Report the malaria status of this cell.
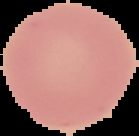

Uninfected.

Summary:
  - Image size: 139×136 pixels
  - Preparation: thin blood film
  - Image type: segmented cell region with the area outside set to black